Locate every leukocyte (white blood cell).
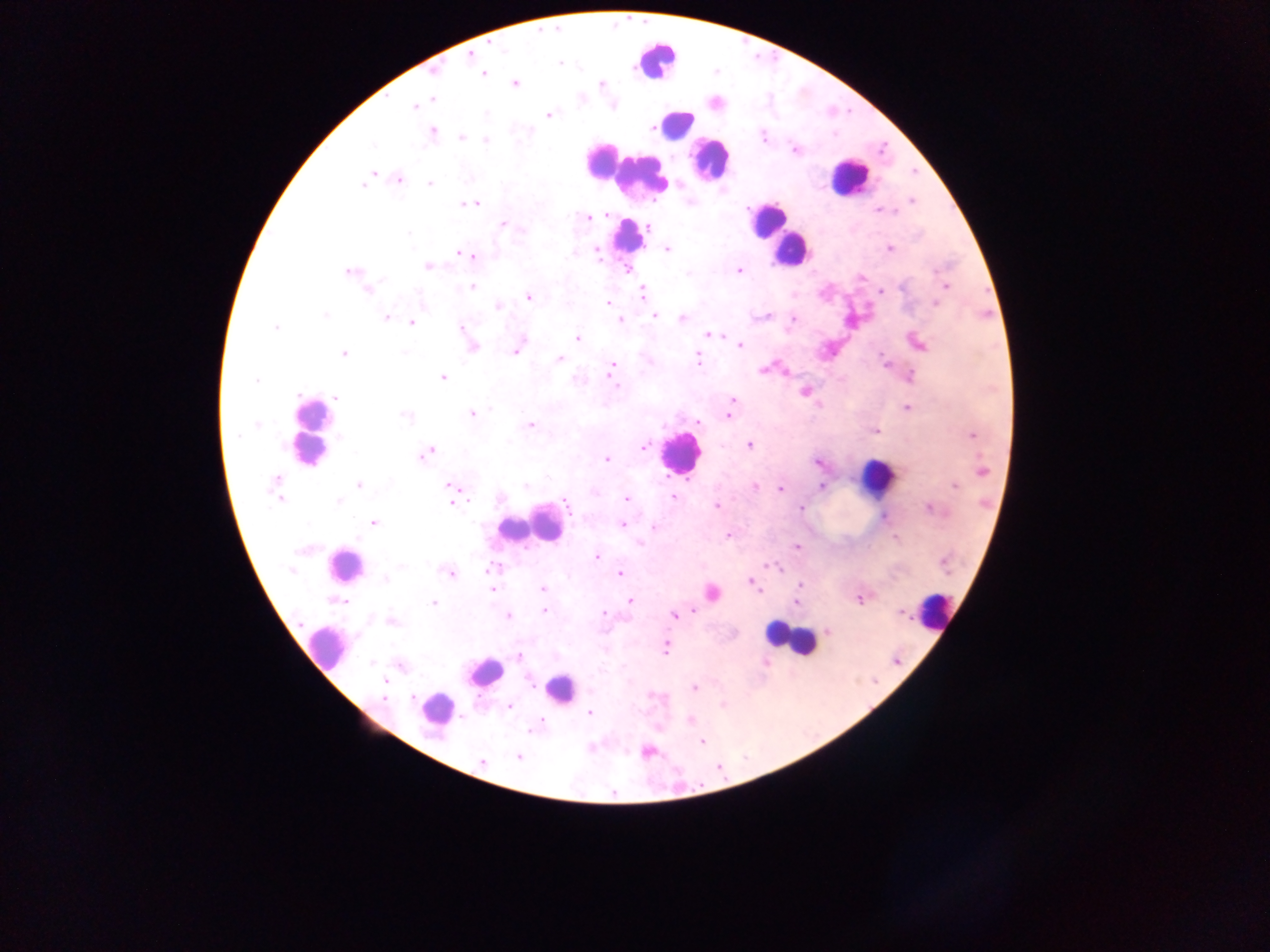

Approximate centers as {x, y} in pixels.
Leukocytes: {657, 59}, {675, 123}, {602, 160}, {710, 160}, {609, 162}, {634, 172}, {849, 177}, {767, 221}, {782, 234}, {629, 236}, {792, 249}, {311, 431}, {678, 452}, {877, 476}, {540, 523}, {515, 527}, {344, 566}, {935, 611}, {790, 638}, {326, 648}, {485, 671}, {560, 690}, {438, 710}.

{
  "malaria_parasite_locations": "approximate centers as {x, y} in pixels: {471, 54}, {433, 70}, {481, 72}, {514, 83}, {600, 84}, {431, 99}, {416, 105}, {613, 106}, {549, 114}, {431, 131}, {462, 137}, {486, 139}, {795, 150}, {373, 174}, {398, 178}, {366, 180}, {430, 183}, {912, 201}, {471, 203}, {880, 211}, {589, 217}, {504, 225}, {667, 248}, {890, 248}, {597, 250}, {459, 251}, {472, 256}, {428, 266}, {627, 268}, {739, 270}, {350, 271}, {861, 277}, {945, 286}, {472, 287}, {368, 289}, {881, 292}, {642, 293}, {528, 296}, {607, 303}, {935, 304}, {497, 305}, {654, 315}, {386, 317}, {681, 319}, {620, 320}, {411, 322}, {462, 328}, {709, 334}, {577, 337}, {469, 341}, {918, 342}, {740, 344}, {472, 346}, {516, 349}, {343, 352}, {560, 358}, {697, 359}, {886, 363}, {781, 370}, {611, 371}, {909, 376}, {442, 377}, {805, 391}, {337, 397}, {733, 400}, {907, 407}, {472, 414}, {728, 415}, {697, 420}, {529, 424}, {875, 430}, {972, 434}, {749, 444}, {644, 447}, {426, 452}, {606, 459}, {818, 462}, {980, 470}, {359, 486}, {955, 486}, {277, 487}, {755, 487}, {820, 487}, {779, 488}, {452, 489}, {672, 497}, {626, 498}, {452, 502}, {564, 502}, {717, 505}, {929, 507}, {800, 508}, {884, 516}, {373, 522}, {622, 524}, {654, 527}, {727, 535}, {796, 547}, {597, 557}, {449, 573}, {620, 574}, {751, 582}, {799, 584}, {543, 589}, {492, 590}, {711, 593}, {860, 598}, {630, 600}, {796, 601}, {433, 603}, {545, 609}, {604, 613}, {673, 614}, {508, 615}, {391, 621}, {828, 631}, {664, 648}, {519, 655}, {385, 680}, {694, 687}, {509, 706}, {589, 712}, {690, 720}, {539, 722}, {701, 740}, {647, 752}, {518, 756}, {481, 763}",
  "capture": "mobile-phone photograph through a microscope",
  "preparation": "thick blood smear",
  "field_of_view": "single",
  "image_size": "1270×952 pixels",
  "country": "Ghana"
}